Outline each blood parasite and name the species.
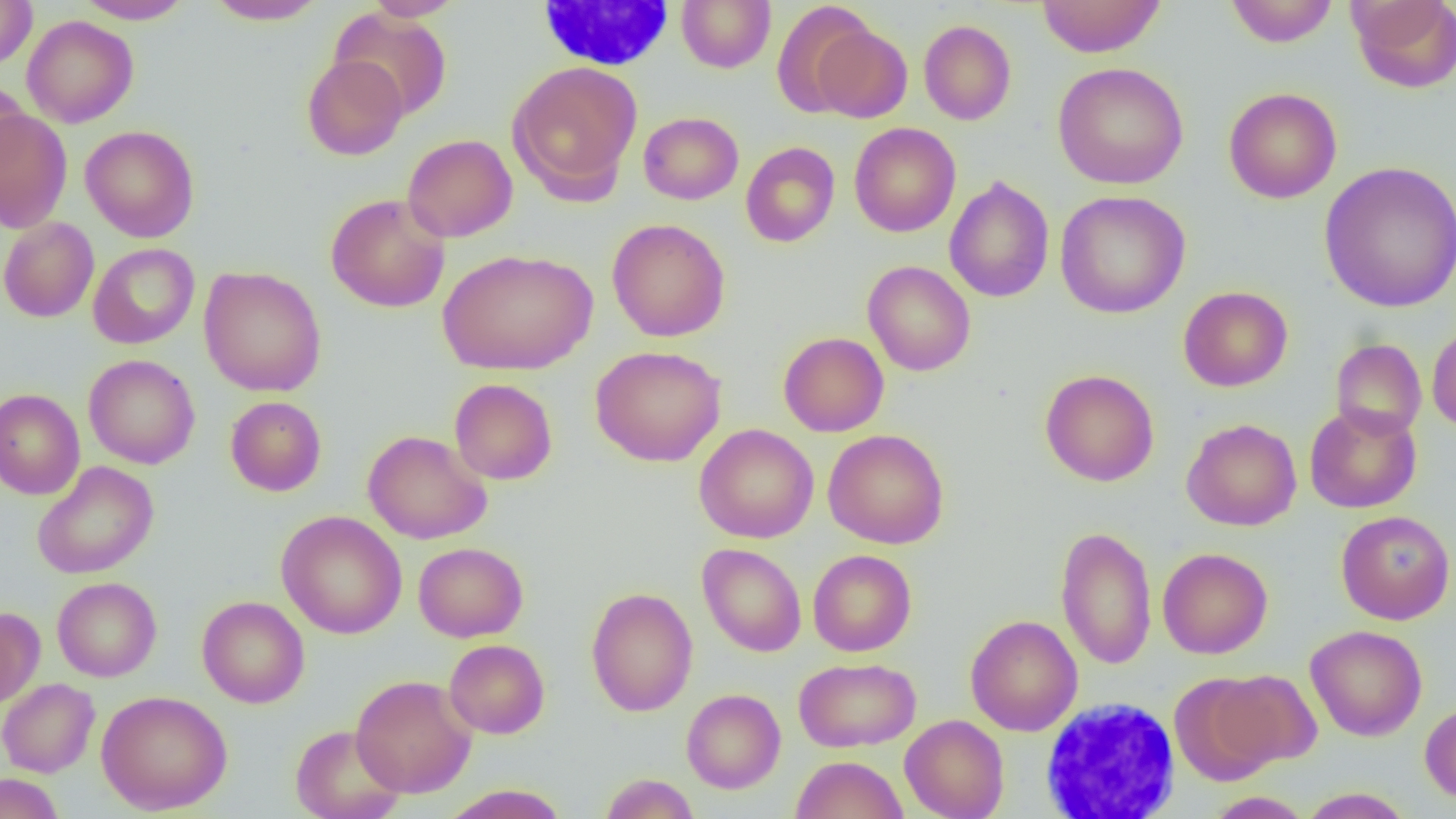

No blood parasites observed.

Approximate bounding boxes as named x1/y1/x2/y2 corners in pixels. Uninfected red blood cell locations: (x1=74, y1=0, x2=194, y2=24), (x1=203, y1=0, x2=329, y2=25), (x1=362, y1=0, x2=465, y2=21), (x1=676, y1=0, x2=776, y2=73), (x1=1036, y1=0, x2=1166, y2=57), (x1=1225, y1=0, x2=1339, y2=47), (x1=1348, y1=0, x2=1456, y2=93), (x1=0, y1=1, x2=37, y2=69), (x1=771, y1=1, x2=877, y2=118), (x1=331, y1=7, x2=453, y2=120), (x1=22, y1=15, x2=138, y2=128), (x1=919, y1=20, x2=1016, y2=125), (x1=813, y1=24, x2=914, y2=123), (x1=302, y1=54, x2=408, y2=160), (x1=507, y1=60, x2=643, y2=201), (x1=1052, y1=62, x2=1189, y2=189), (x1=0, y1=79, x2=30, y2=180), (x1=1223, y1=87, x2=1342, y2=204), (x1=0, y1=109, x2=72, y2=233), (x1=639, y1=112, x2=743, y2=205), (x1=849, y1=122, x2=961, y2=237), (x1=80, y1=125, x2=199, y2=242), (x1=402, y1=134, x2=518, y2=242), (x1=740, y1=141, x2=840, y2=247), (x1=1318, y1=160, x2=1456, y2=313), (x1=944, y1=175, x2=1055, y2=303), (x1=1054, y1=190, x2=1191, y2=319), (x1=325, y1=194, x2=450, y2=313), (x1=0, y1=216, x2=99, y2=322), (x1=607, y1=219, x2=731, y2=342), (x1=87, y1=243, x2=199, y2=349), (x1=438, y1=248, x2=598, y2=375), (x1=862, y1=260, x2=975, y2=376), (x1=198, y1=265, x2=327, y2=397), (x1=1178, y1=286, x2=1293, y2=391), (x1=1427, y1=321, x2=1456, y2=433), (x1=778, y1=332, x2=889, y2=437), (x1=1330, y1=339, x2=1427, y2=440), (x1=590, y1=345, x2=726, y2=467), (x1=83, y1=354, x2=200, y2=469), (x1=1040, y1=369, x2=1159, y2=486), (x1=449, y1=379, x2=557, y2=485), (x1=0, y1=389, x2=85, y2=500), (x1=225, y1=396, x2=326, y2=496), (x1=1304, y1=403, x2=1422, y2=513), (x1=1181, y1=418, x2=1302, y2=531), (x1=694, y1=423, x2=819, y2=543), (x1=823, y1=429, x2=949, y2=549), (x1=363, y1=430, x2=492, y2=544), (x1=32, y1=461, x2=159, y2=579), (x1=277, y1=510, x2=407, y2=639), (x1=1336, y1=510, x2=1455, y2=625), (x1=1055, y1=525, x2=1157, y2=670), (x1=413, y1=542, x2=528, y2=642), (x1=697, y1=543, x2=807, y2=657), (x1=1157, y1=547, x2=1273, y2=659), (x1=808, y1=549, x2=917, y2=656), (x1=52, y1=577, x2=162, y2=682), (x1=585, y1=587, x2=698, y2=717), (x1=197, y1=595, x2=310, y2=708), (x1=0, y1=607, x2=44, y2=707), (x1=965, y1=615, x2=1083, y2=735), (x1=1305, y1=624, x2=1427, y2=741), (x1=444, y1=639, x2=550, y2=739), (x1=793, y1=656, x2=921, y2=752), (x1=1212, y1=670, x2=1322, y2=769), (x1=1169, y1=673, x2=1281, y2=785), (x1=351, y1=674, x2=478, y2=798), (x1=0, y1=678, x2=100, y2=778), (x1=681, y1=688, x2=786, y2=793), (x1=96, y1=690, x2=232, y2=814), (x1=1420, y1=701, x2=1456, y2=805), (x1=900, y1=714, x2=1010, y2=818), (x1=291, y1=725, x2=406, y2=819), (x1=791, y1=755, x2=908, y2=819), (x1=0, y1=772, x2=64, y2=819), (x1=599, y1=773, x2=700, y2=818), (x1=440, y1=784, x2=571, y2=819), (x1=1298, y1=787, x2=1414, y2=818), (x1=1204, y1=791, x2=1313, y2=818). White blood cell locations: (x1=534, y1=1, x2=677, y2=72), (x1=1041, y1=697, x2=1181, y2=818). Slide-level diagnosis: no evidence of blood parasites. 1000x magnification. Image is 1456×819 pixels. Thin blood film. One field of a larger specimen. Optical microscopy.